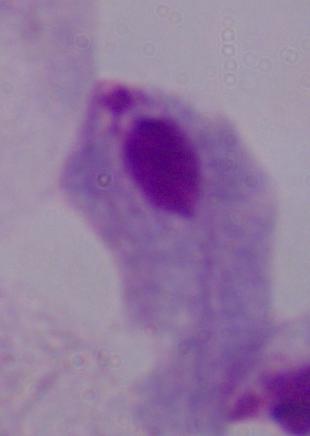 Photomicrograph. Captured at 1000x magnification. A trichomonad is shown.